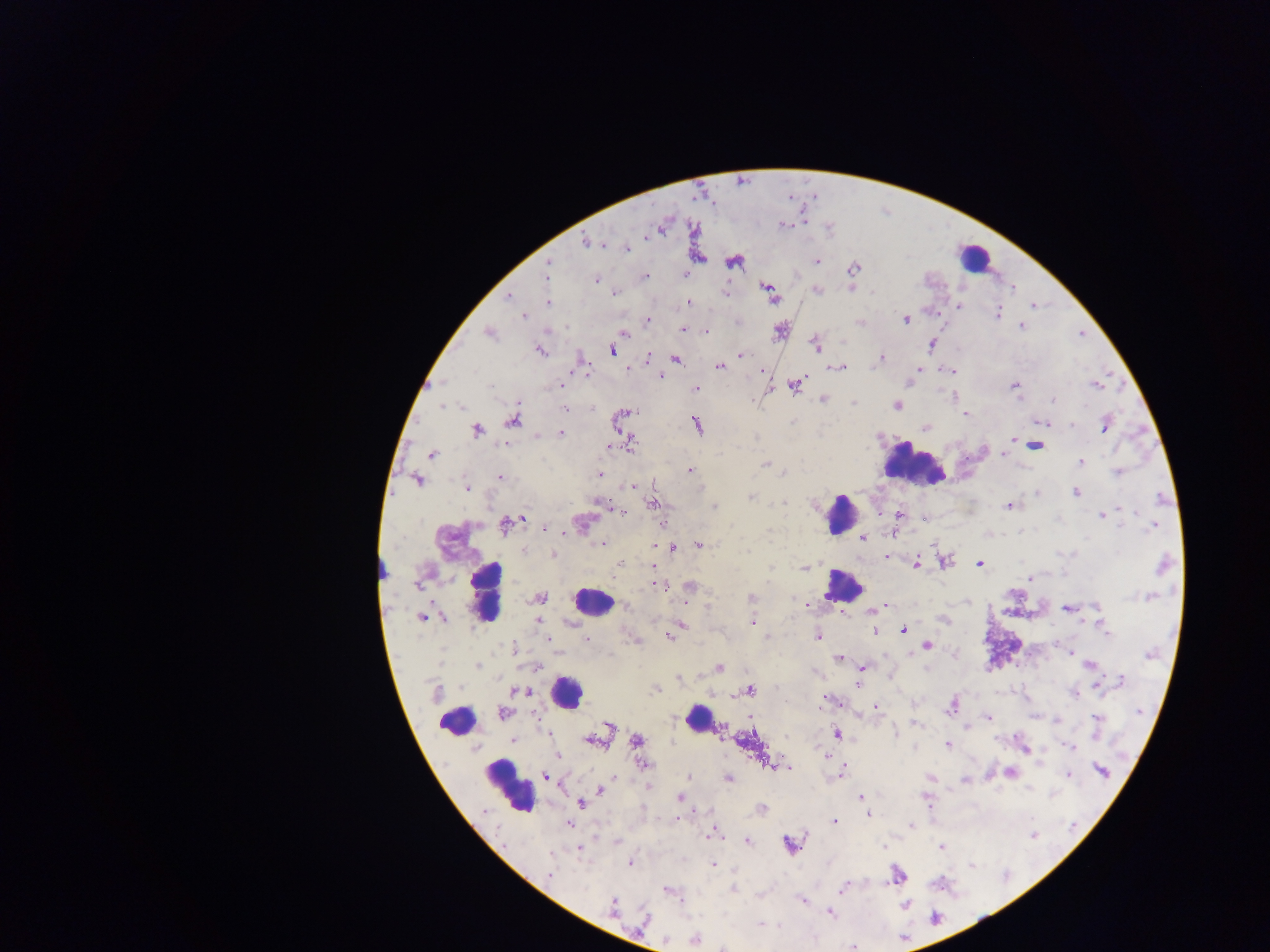

Approximate centers as (x, y) in pixels.
Summary:
  - Leukocyte locations: (973, 257), (914, 464), (840, 514), (842, 585), (487, 592), (592, 601), (566, 693), (698, 719), (457, 720), (509, 787)
  - Malaria parasite locations: (782, 225), (586, 241), (627, 247), (817, 261), (733, 262), (548, 265), (853, 269), (686, 274), (546, 276), (644, 276), (596, 280), (816, 291), (769, 292), (616, 293), (725, 293), (508, 296), (548, 302), (690, 302), (959, 306), (1033, 306), (998, 314), (523, 316), (906, 319), (648, 320), (860, 322), (1021, 326), (683, 330), (780, 330), (706, 331), (624, 333), (490, 334), (816, 344), (931, 344), (541, 350), (612, 351), (742, 355), (648, 358), (881, 358), (675, 359), (719, 366), (840, 367), (918, 369), (951, 371), (660, 377), (442, 382), (559, 385), (795, 385), (1015, 385), (1096, 385), (490, 386), (695, 388), (823, 399), (1053, 399), (853, 402), (443, 406), (897, 406), (461, 407), (592, 408), (565, 410), (629, 413), (966, 414), (512, 420), (1042, 422), (697, 425), (1072, 425), (1105, 426), (925, 427), (477, 431), (560, 433), (536, 435), (1012, 440), (504, 444), (609, 445), (632, 445), (1035, 446), (432, 454), (1003, 455), (1080, 462), (766, 463), (689, 470), (1117, 472), (599, 474), (783, 474), (501, 477), (417, 480), (632, 486), (467, 488), (1076, 492), (1037, 493), (750, 497), (783, 503), (598, 504), (652, 504), (1009, 506), (715, 507), (1120, 508), (623, 512), (879, 514), (899, 515), (1102, 515), (523, 517), (925, 518), (581, 523), (505, 525), (1152, 526), (546, 528), (862, 539), (602, 544), (699, 544), (655, 545), (672, 548), (524, 550), (553, 555), (887, 557), (944, 562), (980, 563), (620, 564), (916, 564), (1163, 564), (654, 566), (804, 569), (1031, 579), (418, 585), (659, 585), (689, 585), (751, 597), (1149, 597), (540, 598), (804, 604), (882, 607), (1097, 607), (627, 608), (1067, 609), (874, 610), (422, 618), (445, 619), (943, 619), (537, 621), (752, 623), (680, 625), (903, 629), (876, 631), (1107, 631), (671, 635), (818, 636), (766, 637), (586, 639), (548, 640), (927, 645), (513, 649), (1069, 652), (1150, 655), (839, 659), (1090, 665), (478, 666), (538, 666), (862, 667), (719, 668), (679, 678), (1122, 681), (858, 683), (1098, 684), (654, 690), (750, 690), (521, 691), (436, 693), (1074, 694), (823, 701), (951, 707), (877, 708), (1139, 712), (503, 714), (988, 716), (1097, 718), (917, 724), (609, 726), (894, 733), (837, 735), (512, 740), (592, 740), (637, 740), (948, 745), (1069, 746), (558, 755), (644, 765), (777, 766), (784, 767), (1101, 771), (1011, 773), (842, 774), (1069, 775), (547, 777), (689, 777), (930, 777), (728, 779), (964, 779), (648, 786), (601, 790), (679, 797), (861, 797), (581, 804), (762, 808), (869, 814), (835, 822), (569, 824), (911, 825), (712, 835), (1034, 835), (616, 841), (748, 841), (790, 844), (883, 846), (940, 847), (579, 849), (551, 856), (629, 863), (714, 864), (971, 865), (550, 874), (897, 876), (733, 889), (842, 889), (668, 892), (802, 901), (905, 905), (612, 906), (830, 913), (934, 917), (645, 919), (761, 925), (695, 938), (853, 947), (724, 948)
  - Country: Ghana
  - Capture: mobile-phone photograph through a microscope
  - Image size: 1270×952 pixels
  - Field of view: single
  - Preparation: thick blood film